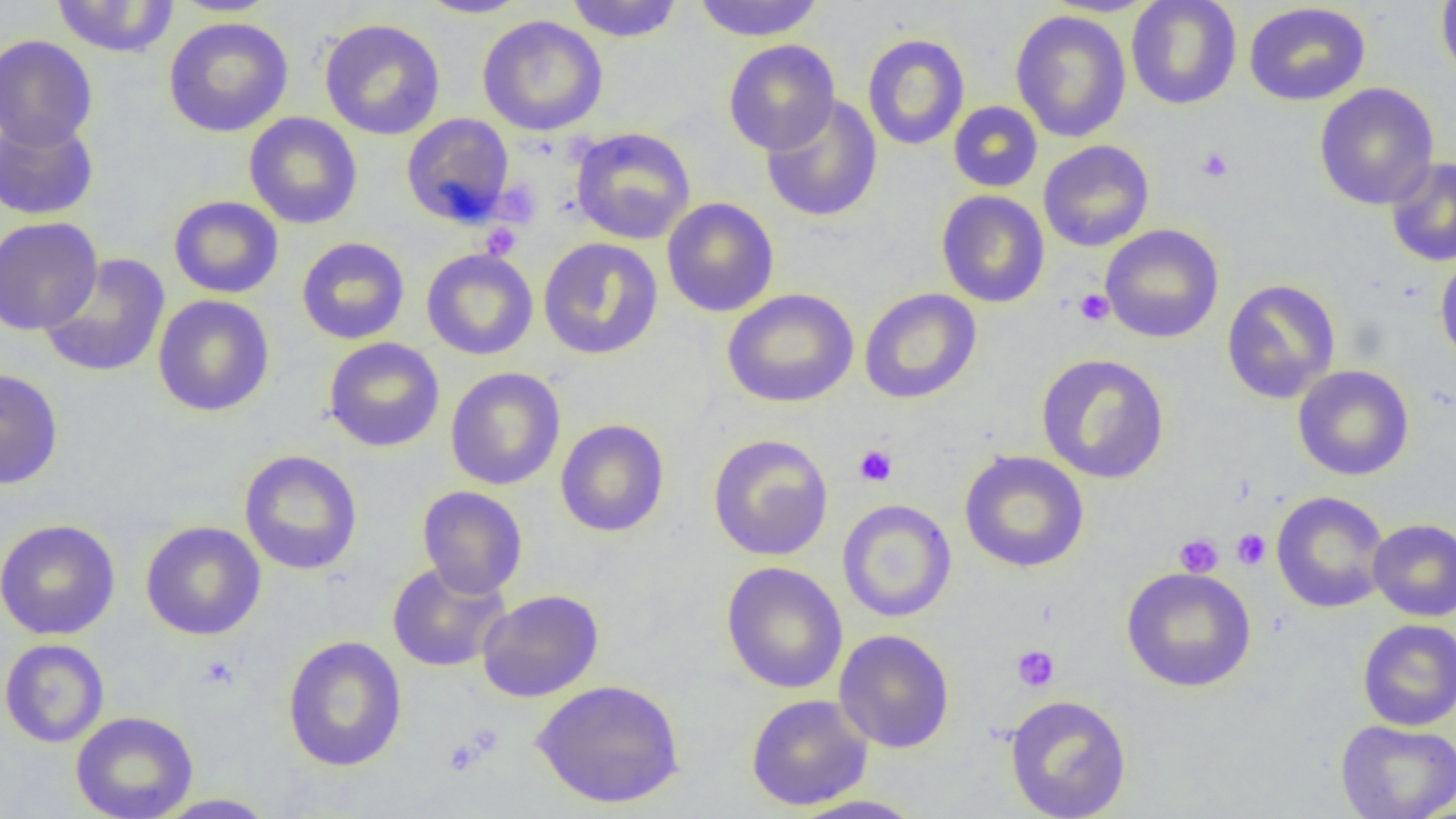 Approximate bounding boxes as named x1/y1/x2/y2 corners in pixels. Platelet locations: (x1=1196, y1=146, x2=1235, y2=183), (x1=495, y1=181, x2=541, y2=227), (x1=481, y1=223, x2=521, y2=260), (x1=1073, y1=287, x2=1114, y2=327), (x1=854, y1=444, x2=898, y2=487), (x1=1231, y1=529, x2=1271, y2=570), (x1=1174, y1=533, x2=1223, y2=578), (x1=1011, y1=645, x2=1060, y2=692), (x1=196, y1=654, x2=240, y2=691), (x1=443, y1=737, x2=484, y2=776). Uninfected red blood cell locations: (x1=51, y1=0, x2=179, y2=58), (x1=169, y1=0, x2=283, y2=17), (x1=417, y1=0, x2=532, y2=18), (x1=565, y1=0, x2=684, y2=43), (x1=691, y1=0, x2=826, y2=41), (x1=1126, y1=0, x2=1242, y2=110), (x1=1435, y1=0, x2=1456, y2=84), (x1=1243, y1=2, x2=1371, y2=106), (x1=1010, y1=9, x2=1131, y2=143), (x1=477, y1=15, x2=608, y2=136), (x1=163, y1=16, x2=294, y2=138), (x1=319, y1=18, x2=446, y2=141), (x1=862, y1=33, x2=970, y2=150), (x1=0, y1=34, x2=98, y2=150), (x1=723, y1=39, x2=840, y2=155), (x1=1314, y1=83, x2=1439, y2=210), (x1=761, y1=95, x2=883, y2=222), (x1=948, y1=101, x2=1043, y2=193), (x1=244, y1=113, x2=363, y2=229), (x1=401, y1=113, x2=515, y2=228), (x1=0, y1=115, x2=99, y2=220), (x1=569, y1=127, x2=696, y2=244), (x1=1038, y1=140, x2=1154, y2=252), (x1=1385, y1=156, x2=1456, y2=268), (x1=936, y1=190, x2=1050, y2=308), (x1=169, y1=195, x2=284, y2=299), (x1=662, y1=197, x2=779, y2=317), (x1=0, y1=216, x2=102, y2=335), (x1=1100, y1=224, x2=1224, y2=344), (x1=296, y1=237, x2=410, y2=344), (x1=538, y1=237, x2=663, y2=360), (x1=421, y1=248, x2=538, y2=360), (x1=1434, y1=253, x2=1456, y2=369), (x1=38, y1=254, x2=170, y2=378), (x1=1222, y1=279, x2=1341, y2=404), (x1=722, y1=287, x2=859, y2=408), (x1=859, y1=287, x2=982, y2=405), (x1=152, y1=295, x2=275, y2=417), (x1=323, y1=337, x2=445, y2=452), (x1=1036, y1=353, x2=1170, y2=484), (x1=1293, y1=365, x2=1414, y2=481), (x1=445, y1=367, x2=566, y2=491), (x1=0, y1=368, x2=64, y2=490), (x1=556, y1=419, x2=669, y2=537), (x1=708, y1=433, x2=833, y2=561), (x1=239, y1=449, x2=362, y2=575), (x1=959, y1=450, x2=1089, y2=573), (x1=416, y1=486, x2=528, y2=599), (x1=1271, y1=491, x2=1391, y2=614), (x1=837, y1=499, x2=956, y2=623), (x1=1368, y1=518, x2=1456, y2=621), (x1=0, y1=519, x2=120, y2=640), (x1=140, y1=521, x2=266, y2=641), (x1=386, y1=561, x2=511, y2=672), (x1=721, y1=562, x2=848, y2=694), (x1=1121, y1=566, x2=1257, y2=692), (x1=477, y1=589, x2=604, y2=702), (x1=1357, y1=619, x2=1456, y2=731), (x1=834, y1=629, x2=955, y2=754), (x1=282, y1=635, x2=408, y2=771), (x1=0, y1=638, x2=109, y2=747), (x1=530, y1=679, x2=685, y2=810), (x1=745, y1=693, x2=873, y2=811), (x1=1004, y1=694, x2=1132, y2=819), (x1=70, y1=710, x2=199, y2=819), (x1=1335, y1=719, x2=1456, y2=819), (x1=152, y1=793, x2=279, y2=818), (x1=785, y1=794, x2=929, y2=818). Slide-level diagnosis: no evidence of blood parasites. Thin blood film. One field of a larger specimen. Image is 1456×819 pixels. Light microscopy. 1000x magnification.